Assess the morphology of the erythrocytes.
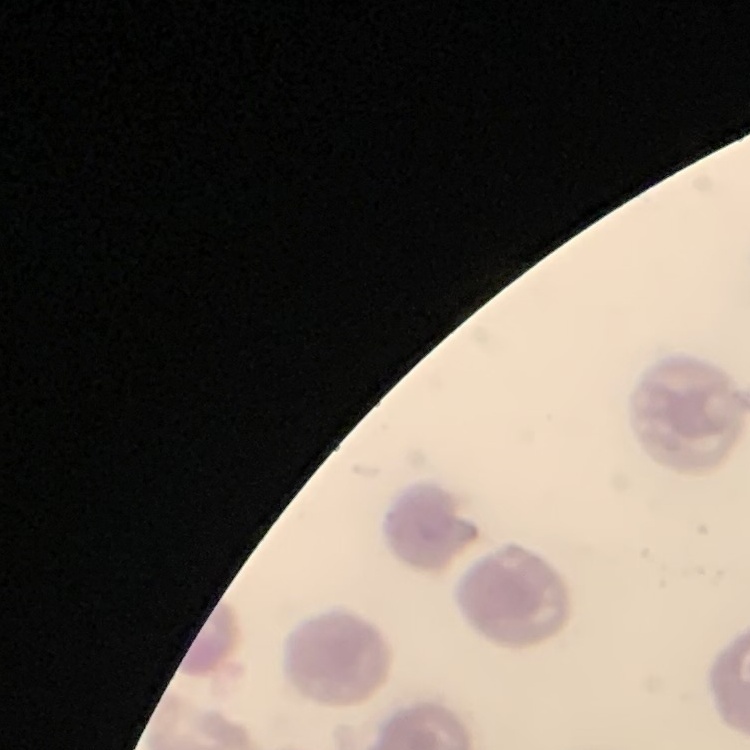

They show no rouleaux formation.

Thin peripheral smear. Stained with either Field's or Giemsa. One tile cut from a larger photomicrograph.